Outline each Plasmodium malariae-infected red blood cell.
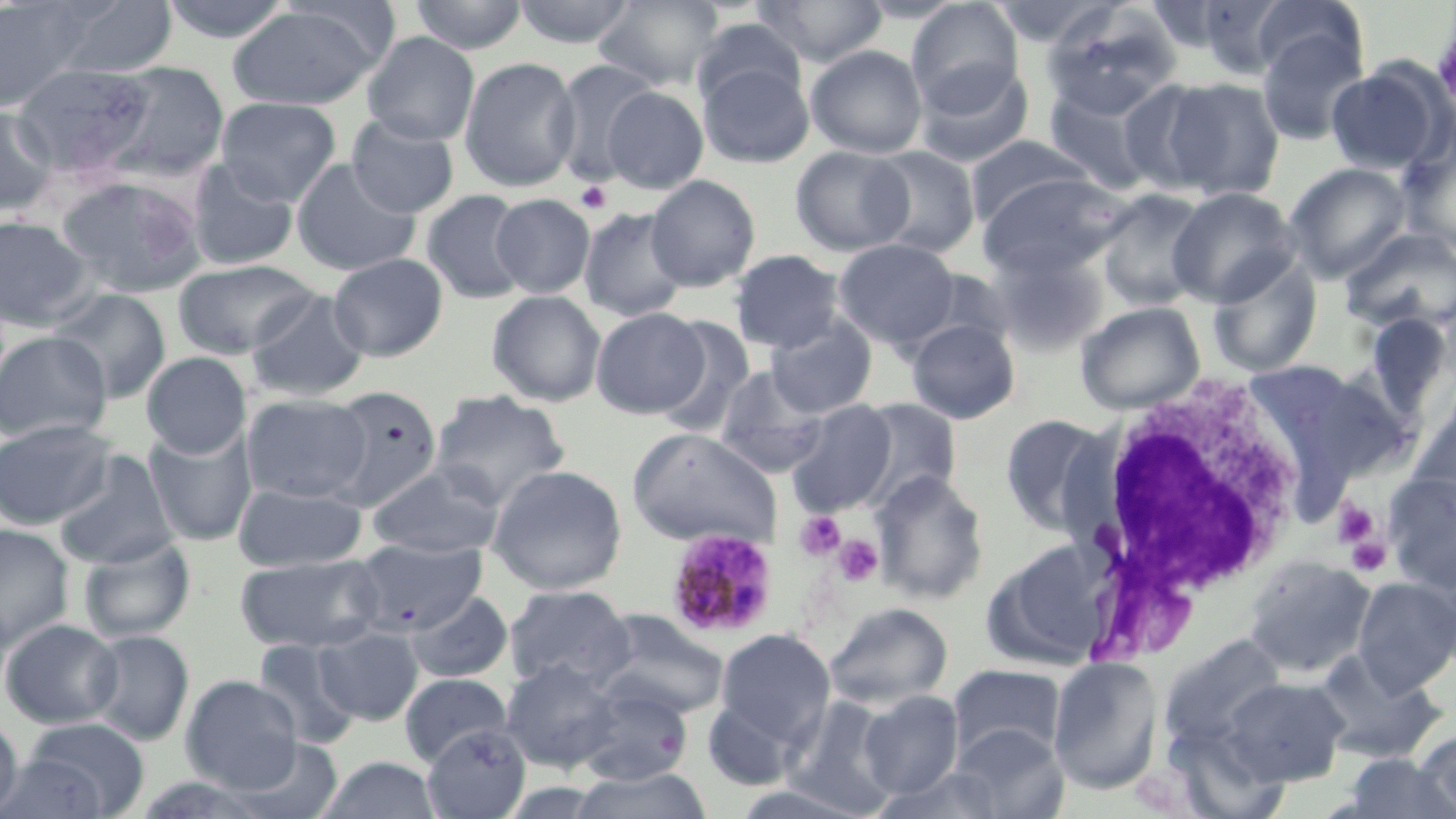
Approximate bounding boxes as (x1, y1, x2, y2) in pixels.
Plasmodium malariae-infected red blood cells: (666, 528, 779, 640).

Summary:
  - Uninfected red blood cell locations: (49, 0, 179, 79), (158, 0, 296, 43), (407, 0, 529, 54), (512, 0, 637, 47), (593, 0, 724, 90), (752, 0, 888, 67), (987, 0, 1123, 47), (1194, 0, 1298, 78), (0, 1, 102, 112), (906, 1, 1023, 112), (1247, 1, 1365, 83), (228, 4, 386, 110), (1042, 7, 1180, 121), (690, 18, 808, 113), (1255, 25, 1368, 146), (362, 32, 479, 145), (806, 45, 928, 158), (458, 55, 581, 192), (552, 58, 661, 186), (697, 60, 814, 168), (914, 60, 1034, 169), (98, 61, 230, 181), (10, 63, 156, 177), (1326, 63, 1447, 175), (1159, 76, 1286, 201), (1120, 77, 1236, 196), (1042, 80, 1165, 195), (602, 86, 708, 194), (215, 96, 342, 205), (0, 106, 59, 217), (346, 115, 460, 218), (1398, 132, 1456, 255), (965, 135, 1092, 228), (790, 146, 914, 256), (867, 146, 980, 258), (185, 158, 300, 271), (291, 158, 420, 276), (1285, 163, 1412, 282), (976, 172, 1129, 278), (55, 175, 207, 298), (646, 175, 760, 291), (1167, 186, 1300, 307), (1094, 189, 1213, 311), (421, 190, 531, 304), (491, 194, 595, 298), (579, 207, 688, 322), (0, 216, 94, 330), (1338, 227, 1456, 336), (834, 238, 960, 348), (989, 246, 1110, 356), (728, 249, 846, 353), (327, 252, 448, 361), (1206, 256, 1323, 379), (173, 259, 320, 358), (48, 287, 172, 403), (246, 289, 370, 401), (487, 290, 607, 407), (1075, 301, 1206, 414), (591, 307, 708, 417), (1355, 309, 1455, 429), (653, 316, 755, 438), (765, 316, 878, 417), (906, 319, 1020, 423), (0, 330, 111, 443), (141, 352, 251, 458), (1239, 359, 1396, 500), (713, 365, 829, 477), (324, 385, 443, 509), (429, 389, 571, 510), (241, 393, 370, 503), (1408, 397, 1455, 519), (854, 398, 961, 507), (785, 400, 899, 515), (999, 414, 1116, 539), (0, 419, 115, 529), (143, 425, 258, 546), (627, 427, 782, 549), (53, 450, 178, 569), (365, 463, 504, 558), (486, 464, 628, 595), (871, 470, 990, 604), (1383, 474, 1455, 593), (233, 482, 366, 572), (0, 523, 75, 651), (77, 534, 196, 643), (351, 538, 488, 637), (981, 540, 1113, 671), (235, 554, 385, 653), (1242, 555, 1377, 678), (1352, 577, 1456, 695), (503, 585, 634, 690), (406, 590, 514, 683), (823, 602, 952, 710), (591, 611, 730, 720), (0, 618, 122, 728), (314, 627, 423, 725), (714, 629, 836, 750), (85, 630, 195, 746), (1158, 633, 1290, 757), (253, 639, 362, 748), (1310, 648, 1448, 764), (1048, 657, 1163, 795), (500, 658, 622, 772), (947, 664, 1067, 764), (399, 673, 513, 767), (181, 674, 303, 792), (1223, 675, 1351, 785), (574, 684, 694, 786), (858, 691, 964, 799), (702, 698, 801, 790), (785, 698, 901, 817), (0, 713, 22, 816), (20, 717, 149, 817), (422, 724, 531, 819), (950, 724, 1068, 818), (1415, 728, 1456, 817), (223, 735, 347, 819), (0, 753, 111, 819), (1340, 753, 1453, 819), (317, 756, 442, 818), (870, 765, 1014, 819), (568, 766, 714, 819)
  - White blood cell locations: (1076, 375, 1310, 621)
  - Platelet locations: (575, 181, 612, 214), (1332, 498, 1379, 548), (794, 511, 845, 561), (835, 535, 883, 587), (1345, 536, 1391, 577)
  - Slide-level diagnosis: Plasmodium malariae
  - Image size: 1456×819 pixels
  - Stain: May-Grünwald-Giemsa
  - Magnification: 1000x
  - Preparation: thin blood film
  - Modality: light microscopy
  - Field of view: single